Classify this cell by malaria status.
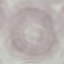
Uninfected.

Thin blood smear. Cell patch, automatically extracted from a larger field of view and resized to 64 × 64 pixels. Giemsa stain. Acquired by smartphone through the microscope eyepiece.